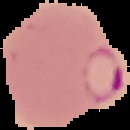

Summary:
  - Image type: cell region segmented out of the field of view; surrounding area masked to black
  - Malaria status: parasitized
  - Preparation: thin blood smear
  - Image size: 130×130 pixels